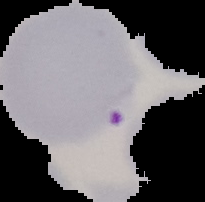

Summary:
  - Preparation: thin blood film
  - Image size: 205×202 pixels
  - Image type: segmented cell region with the area outside set to black
  - Result: malaria parasites detected